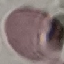 Result: no malaria parasites detected. Acquired by smartphone through the microscope eyepiece. Automatically extracted cell patch, resized to 64 × 64 pixels. Giemsa stain. Thin blood smear.